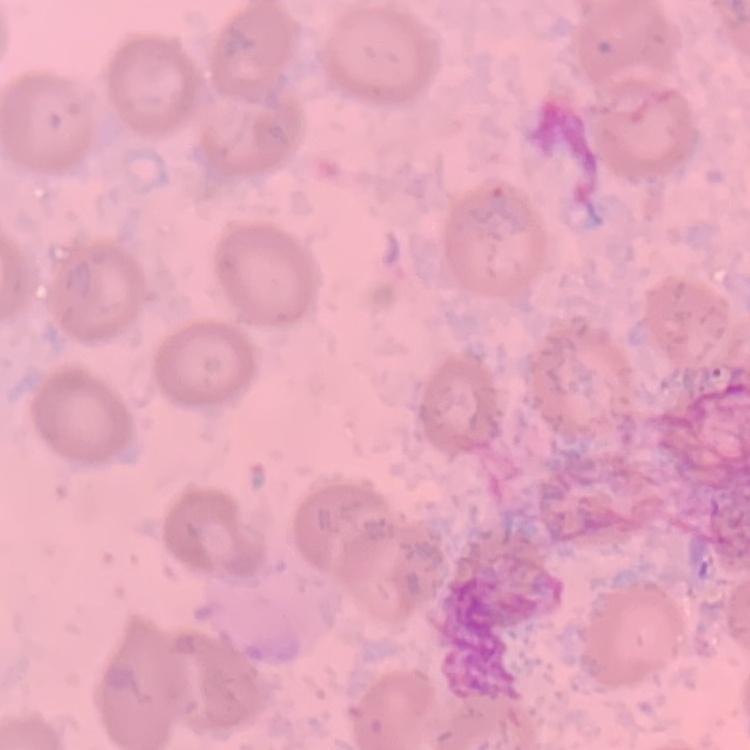 The red blood cells show no rouleaux formation. Square crop of a larger photomicrograph. Thin peripheral smear. Stained with either Field's or Giemsa.